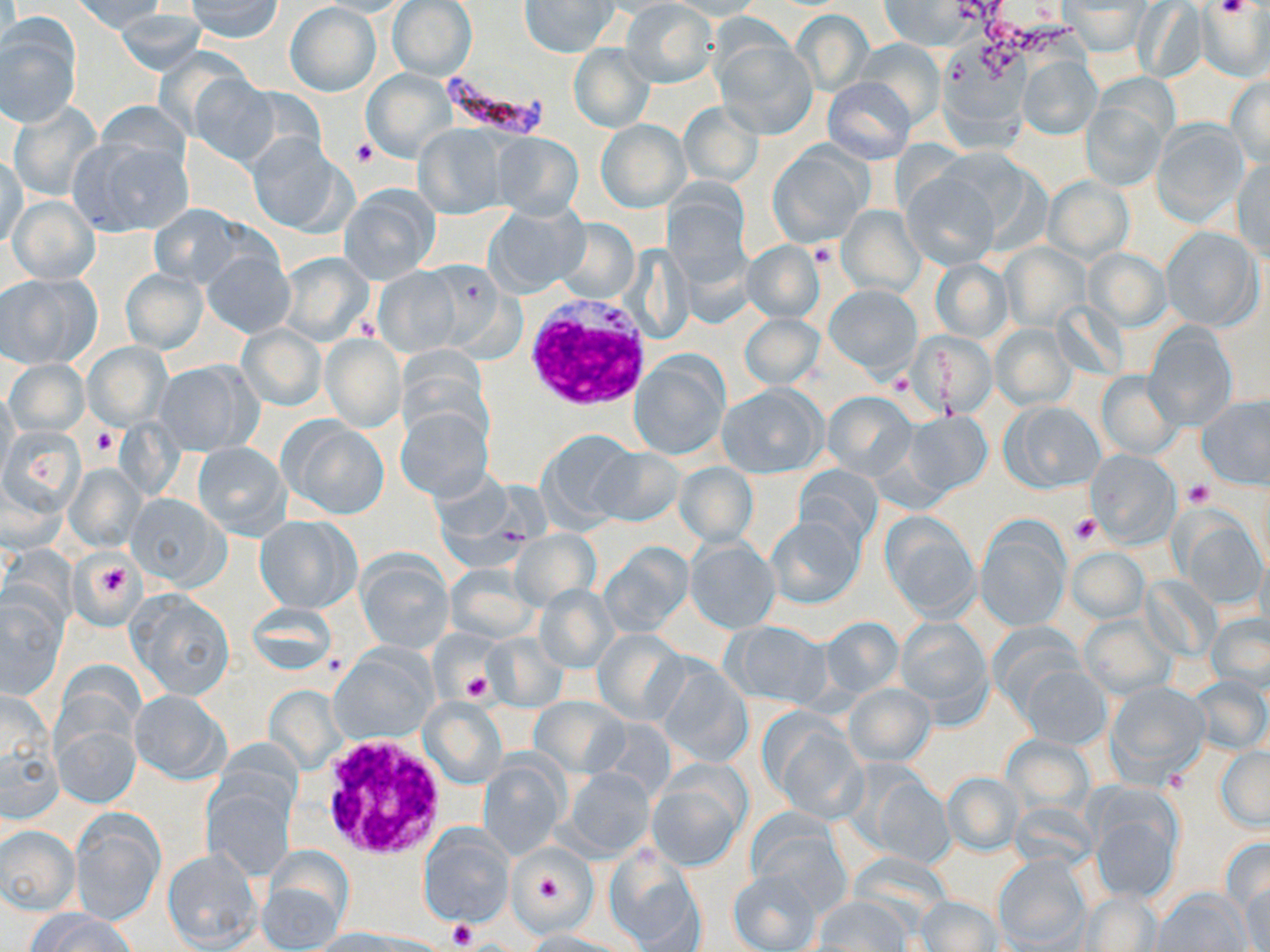

{
  "slide_level_diagnosis": "Plasmodium falciparum",
  "platelet_locations": "approximate bounding boxes as [x1, y1, x2, y2] in pixels: [1215, 0, 1252, 19], [352, 139, 377, 166], [808, 242, 837, 268], [91, 428, 119, 457], [1185, 482, 1214, 508], [1071, 514, 1102, 546], [90, 554, 137, 604], [462, 672, 495, 703], [447, 918, 476, 949]",
  "image_size": "1270×952 pixels",
  "preparation": "thin blood film",
  "stain": "May-Grünwald-Giemsa",
  "uninfected_red_blood_cell_locations": "approximate bounding boxes as [x1, y1, x2, y2] in pixels: [69, 0, 167, 34], [182, 0, 285, 41], [388, 0, 477, 79], [519, 0, 618, 57], [314, 1, 414, 17], [667, 1, 765, 20], [620, 2, 718, 88], [879, 2, 978, 50], [1133, 2, 1206, 84], [286, 3, 381, 97], [1064, 3, 1151, 54], [1194, 3, 1270, 80], [115, 8, 206, 74], [793, 11, 874, 94], [0, 15, 82, 126], [715, 38, 818, 138], [856, 39, 945, 128], [569, 44, 654, 133], [1019, 56, 1100, 139], [362, 69, 455, 162], [188, 76, 283, 168], [824, 76, 915, 165], [1225, 77, 1270, 169], [1083, 99, 1166, 192], [7, 102, 99, 200], [679, 102, 762, 187], [596, 119, 688, 213], [1151, 120, 1250, 227], [415, 124, 509, 219], [64, 132, 193, 237], [246, 133, 348, 234], [491, 133, 584, 220], [769, 144, 870, 248], [1, 153, 26, 252], [1232, 158, 1270, 260], [902, 170, 1001, 270], [1042, 176, 1133, 264], [665, 183, 752, 291], [338, 184, 440, 284], [8, 195, 99, 283], [483, 203, 586, 298], [148, 205, 248, 289], [836, 206, 926, 296], [553, 218, 639, 305], [1160, 227, 1261, 330], [742, 241, 825, 322], [1003, 243, 1091, 332], [1084, 248, 1170, 330], [201, 249, 295, 339], [277, 252, 374, 347], [930, 259, 1011, 341], [374, 266, 464, 356], [121, 268, 208, 355], [0, 274, 98, 368], [826, 285, 922, 376], [740, 313, 824, 388], [1144, 323, 1237, 430], [990, 324, 1075, 409], [237, 325, 326, 411], [905, 331, 997, 418], [321, 335, 405, 432], [83, 343, 171, 429], [629, 350, 729, 460], [6, 359, 89, 436], [152, 361, 261, 456], [1095, 372, 1179, 460], [719, 384, 827, 478], [0, 388, 18, 484], [824, 391, 915, 479], [1197, 397, 1270, 490], [1001, 401, 1104, 493], [395, 405, 493, 502], [902, 411, 992, 498], [280, 418, 389, 519], [2, 427, 78, 523], [537, 429, 639, 527], [193, 442, 290, 539], [591, 447, 684, 527], [1084, 449, 1180, 547], [674, 463, 758, 546], [64, 464, 144, 550], [795, 465, 882, 548], [126, 493, 229, 589], [1176, 508, 1268, 607], [881, 511, 979, 619], [255, 514, 359, 613], [766, 515, 864, 609], [975, 519, 1070, 633], [511, 530, 601, 609], [685, 539, 780, 633], [600, 542, 693, 637], [1067, 548, 1148, 623], [73, 553, 140, 625], [357, 553, 454, 653], [445, 565, 538, 643], [535, 585, 619, 673], [128, 591, 234, 700], [0, 595, 66, 697], [247, 602, 338, 674], [1207, 613, 1270, 695], [1081, 615, 1174, 698], [817, 617, 904, 700], [894, 617, 993, 720], [724, 621, 832, 708], [988, 625, 1089, 718], [593, 628, 689, 724], [483, 635, 567, 711], [331, 646, 436, 744], [655, 659, 754, 767], [1022, 666, 1110, 748], [1189, 675, 1270, 756], [1107, 681, 1210, 780], [844, 683, 935, 766], [1, 689, 61, 817], [129, 689, 229, 782], [51, 695, 142, 808], [530, 696, 628, 776], [420, 699, 506, 789], [764, 715, 867, 823], [1002, 734, 1094, 817], [1217, 748, 1270, 828], [479, 757, 565, 858], [562, 768, 655, 859], [647, 769, 748, 870], [864, 770, 954, 869], [942, 772, 1023, 855], [204, 784, 295, 879], [1090, 799, 1182, 906], [69, 809, 163, 924], [748, 822, 852, 919], [418, 825, 513, 926], [1, 826, 80, 913], [1220, 836, 1270, 919], [605, 845, 707, 952], [163, 847, 263, 952], [994, 853, 1089, 951], [256, 854, 350, 952], [728, 866, 822, 952], [1241, 877, 1270, 952], [1153, 889, 1250, 952], [1079, 893, 1162, 951], [913, 895, 1003, 951], [810, 897, 911, 950], [29, 910, 136, 952], [307, 929, 412, 952], [521, 929, 635, 951]",
  "plasmodium_falciparum_infected_red_blood_cell_locations": "approximate bounding boxes as [x1, y1, x2, y2] in pixels: [440, 65, 550, 141]",
  "modality": "optical microscopy",
  "magnification": "1000x",
  "white_blood_cell_locations": "approximate bounding boxes as [x1, y1, x2, y2] in pixels: [521, 296, 654, 416], [318, 737, 447, 861]",
  "field_of_view": "single"
}